Assess this cell for malaria.
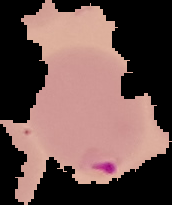

Parasitized.

From a thin blood smear. The area outside the segmented cell region is set to black. Image is 172×205 pixels.